Report the malaria status of this cell.
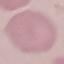

Uninfected.

image type = cell patch, automatically extracted from a larger field of view and resized to 64 × 64 pixels
preparation = thin blood smear
capture = smartphone camera at the microscope eyepiece
stain = Giemsa